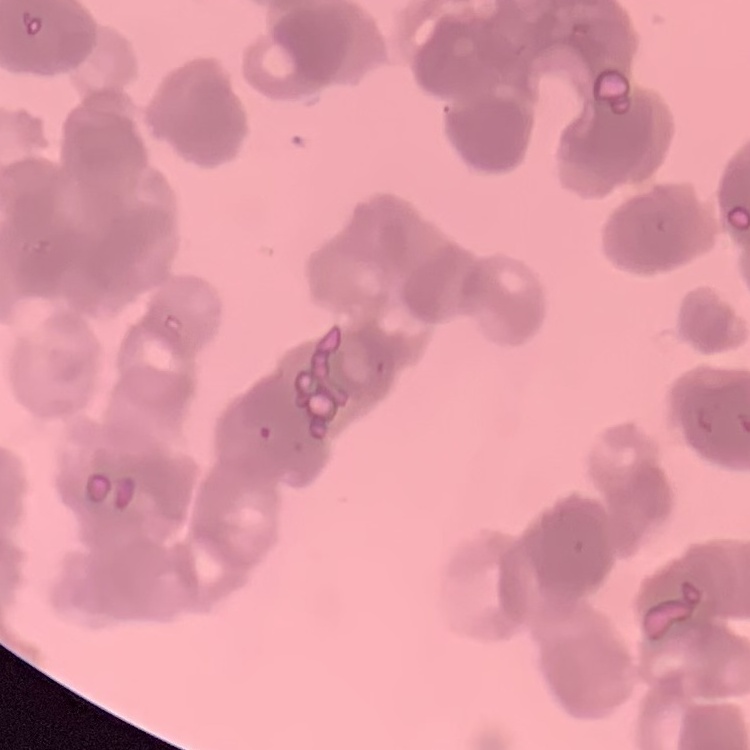 The red blood cells show rouleaux formation. Thin blood film. Stained with either Field's or Giemsa. Square crop of a larger photomicrograph.